Assess this cell for malaria.
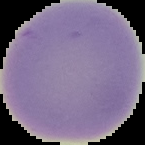

Uninfected.

Image is 145×145 pixels. Cell region segmented out of the field of view; the surrounding area is masked to black. From a thin blood smear.